Comment on the morphology of the erythrocytes.
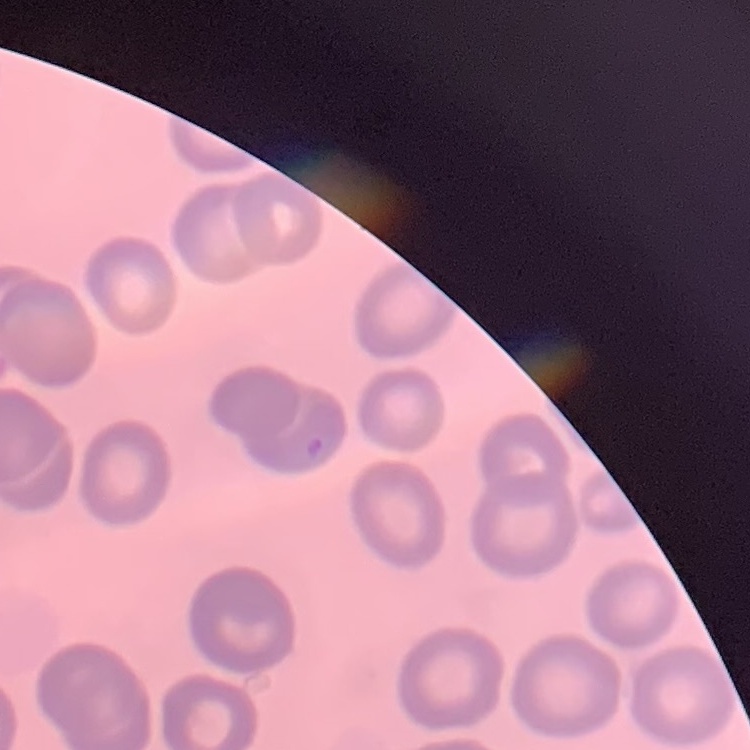

No rouleaux formation.

Field's or Giemsa stain. Thin blood film. Square crop of a larger photomicrograph.